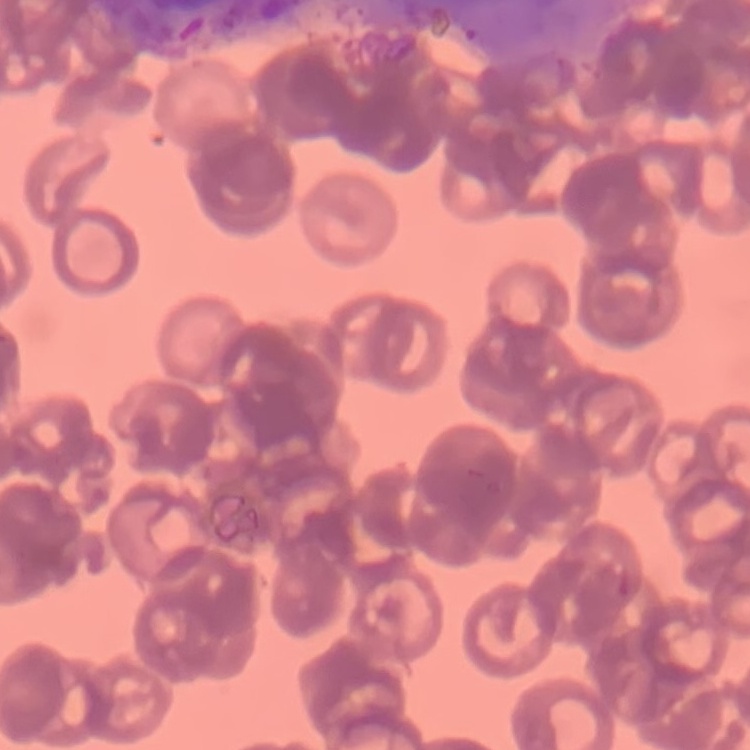
erythrocyte_morphology: rouleaux formation
stain: Field's or Giemsa
preparation: thin blood smear
image_type: square crop of a larger photomicrograph